Locate and identify every blood parasite.
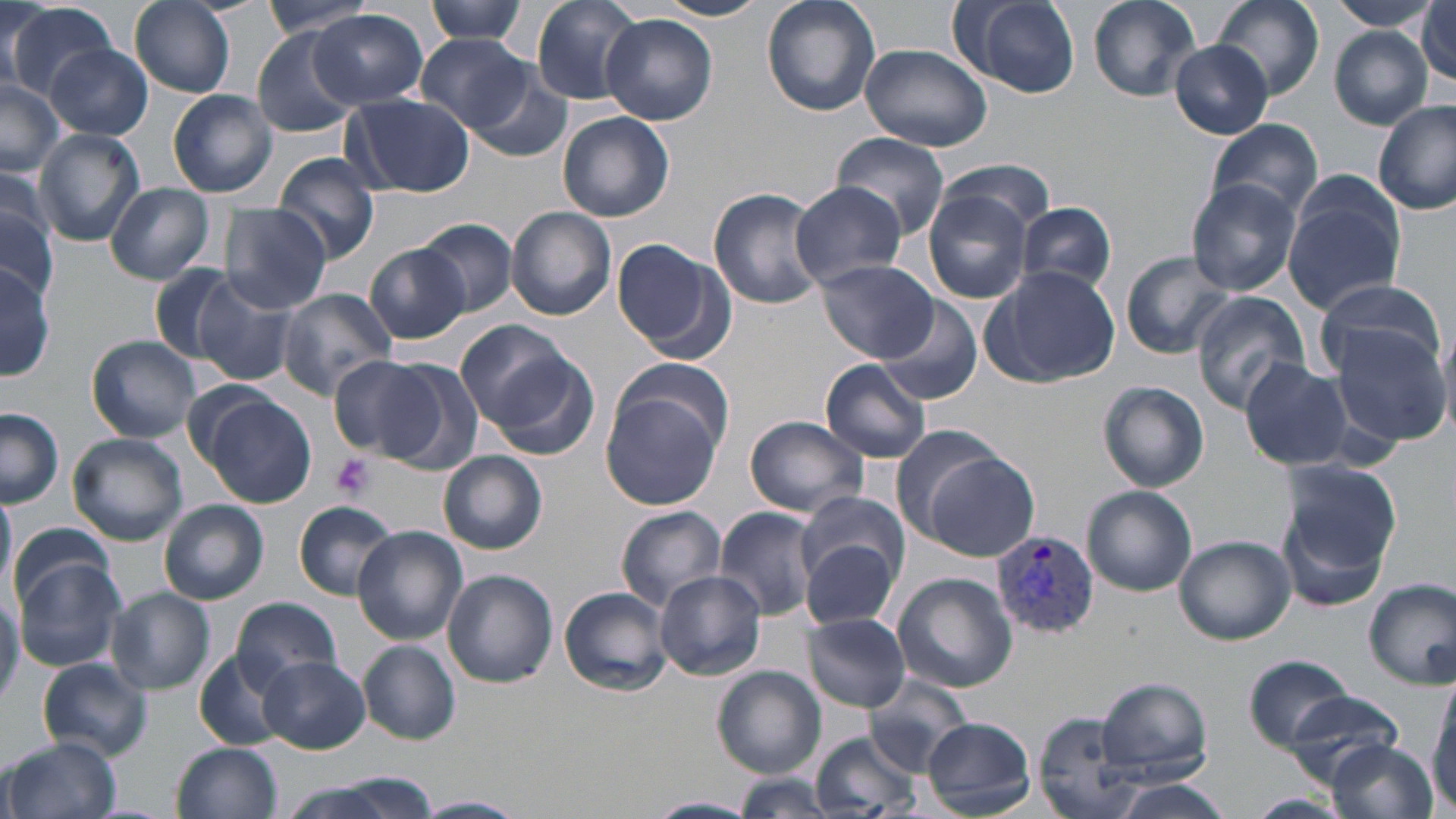
Approximate bounding boxes as named x1/y1/x2/y2 corners in pixels.
Plasmodium vivax-infected red blood cells: (x1=992, y1=531, x2=1100, y2=639).
No Plasmodium falciparum, Plasmodium ovale, Plasmodium malariae, Babesia divergens, or Trypanosoma brucei observed.

slide-level diagnosis = Plasmodium vivax
field of view = one of a larger specimen
modality = optical microscopy
platelet locations = approximate bounding boxes as named x1/y1/x2/y2 corners in pixels: (x1=330, y1=453, x2=374, y2=501)
uninfected red blood cell locations = approximate bounding boxes as named x1/y1/x2/y2 corners in pixels: (x1=129, y1=0, x2=235, y2=99), (x1=261, y1=0, x2=376, y2=38), (x1=423, y1=0, x2=531, y2=45), (x1=529, y1=0, x2=651, y2=106), (x1=651, y1=0, x2=775, y2=21), (x1=762, y1=0, x2=881, y2=117), (x1=1088, y1=0, x2=1202, y2=101), (x1=1210, y1=0, x2=1325, y2=100), (x1=1329, y1=0, x2=1437, y2=30), (x1=947, y1=1, x2=1080, y2=97), (x1=1418, y1=1, x2=1455, y2=86), (x1=7, y1=4, x2=119, y2=104), (x1=311, y1=10, x2=429, y2=110), (x1=602, y1=14, x2=718, y2=126), (x1=252, y1=28, x2=359, y2=137), (x1=1330, y1=28, x2=1433, y2=128), (x1=412, y1=35, x2=533, y2=132), (x1=1170, y1=41, x2=1273, y2=138), (x1=859, y1=43, x2=992, y2=152), (x1=47, y1=44, x2=153, y2=141), (x1=465, y1=65, x2=576, y2=163), (x1=0, y1=79, x2=63, y2=175), (x1=167, y1=89, x2=278, y2=197), (x1=343, y1=92, x2=475, y2=196), (x1=1374, y1=100, x2=1456, y2=216), (x1=558, y1=110, x2=675, y2=223), (x1=1206, y1=119, x2=1323, y2=221), (x1=33, y1=129, x2=144, y2=247), (x1=831, y1=133, x2=949, y2=238), (x1=937, y1=156, x2=1057, y2=233), (x1=272, y1=158, x2=383, y2=262), (x1=0, y1=159, x2=64, y2=260), (x1=1283, y1=175, x2=1407, y2=314), (x1=1187, y1=177, x2=1301, y2=296), (x1=788, y1=182, x2=909, y2=289), (x1=105, y1=186, x2=216, y2=283), (x1=708, y1=187, x2=827, y2=309), (x1=923, y1=188, x2=1034, y2=304), (x1=1017, y1=200, x2=1119, y2=296), (x1=0, y1=203, x2=57, y2=304), (x1=220, y1=204, x2=333, y2=313), (x1=506, y1=208, x2=616, y2=321), (x1=417, y1=220, x2=516, y2=316), (x1=609, y1=238, x2=729, y2=358), (x1=364, y1=243, x2=471, y2=344), (x1=1120, y1=251, x2=1238, y2=358), (x1=817, y1=260, x2=938, y2=362), (x1=0, y1=262, x2=54, y2=380), (x1=150, y1=265, x2=240, y2=361), (x1=983, y1=265, x2=1121, y2=387), (x1=1313, y1=276, x2=1446, y2=376), (x1=192, y1=278, x2=298, y2=386), (x1=274, y1=288, x2=396, y2=399), (x1=1191, y1=293, x2=1310, y2=412), (x1=876, y1=297, x2=982, y2=405), (x1=456, y1=321, x2=582, y2=437), (x1=1330, y1=322, x2=1452, y2=448), (x1=1436, y1=323, x2=1456, y2=441), (x1=87, y1=335, x2=200, y2=442), (x1=484, y1=354, x2=600, y2=464), (x1=327, y1=355, x2=443, y2=460), (x1=1239, y1=357, x2=1356, y2=472), (x1=376, y1=358, x2=484, y2=473), (x1=613, y1=358, x2=733, y2=461), (x1=820, y1=358, x2=933, y2=464), (x1=1098, y1=381, x2=1208, y2=491), (x1=599, y1=388, x2=725, y2=512), (x1=200, y1=393, x2=316, y2=510), (x1=1, y1=409, x2=63, y2=506), (x1=744, y1=415, x2=870, y2=520), (x1=889, y1=424, x2=1016, y2=544), (x1=68, y1=433, x2=188, y2=546), (x1=439, y1=451, x2=547, y2=555), (x1=922, y1=453, x2=1039, y2=562), (x1=1279, y1=461, x2=1400, y2=599), (x1=0, y1=484, x2=16, y2=600), (x1=1082, y1=486, x2=1198, y2=596), (x1=159, y1=499, x2=268, y2=605), (x1=293, y1=501, x2=402, y2=600), (x1=615, y1=505, x2=726, y2=610), (x1=714, y1=508, x2=821, y2=621), (x1=11, y1=522, x2=116, y2=609), (x1=799, y1=524, x2=902, y2=633), (x1=353, y1=526, x2=468, y2=644), (x1=1173, y1=535, x2=1295, y2=645), (x1=13, y1=558, x2=128, y2=672), (x1=442, y1=569, x2=558, y2=688), (x1=654, y1=572, x2=766, y2=682), (x1=892, y1=572, x2=1017, y2=693), (x1=1363, y1=578, x2=1456, y2=688), (x1=559, y1=586, x2=673, y2=696), (x1=106, y1=588, x2=215, y2=695), (x1=232, y1=597, x2=343, y2=695), (x1=804, y1=614, x2=911, y2=713), (x1=202, y1=616, x2=323, y2=730), (x1=359, y1=640, x2=461, y2=744), (x1=194, y1=653, x2=291, y2=751), (x1=1243, y1=655, x2=1357, y2=750), (x1=260, y1=656, x2=371, y2=754), (x1=38, y1=658, x2=153, y2=762), (x1=713, y1=666, x2=825, y2=779), (x1=1424, y1=673, x2=1456, y2=818), (x1=869, y1=674, x2=973, y2=774), (x1=1096, y1=676, x2=1212, y2=780), (x1=1279, y1=693, x2=1408, y2=792), (x1=1036, y1=714, x2=1149, y2=819), (x1=920, y1=715, x2=1035, y2=816), (x1=809, y1=732, x2=921, y2=818), (x1=5, y1=737, x2=122, y2=819), (x1=1327, y1=739, x2=1438, y2=819), (x1=171, y1=742, x2=281, y2=819), (x1=732, y1=775, x2=834, y2=817), (x1=281, y1=778, x2=438, y2=819), (x1=1107, y1=779, x2=1236, y2=819), (x1=1246, y1=793, x2=1355, y2=819), (x1=411, y1=796, x2=527, y2=817), (x1=645, y1=796, x2=760, y2=819)
stain = May-Grünwald-Giemsa
preparation = thin blood film
image size = 1456×819 pixels
magnification = 1000x